Assess this cell for malaria.
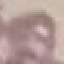

Uninfected.

preparation = thin blood smear
image type = automatically extracted cell patch, resized to 64 × 64 pixels
stain = Giemsa
capture = smartphone camera at the microscope eyepiece